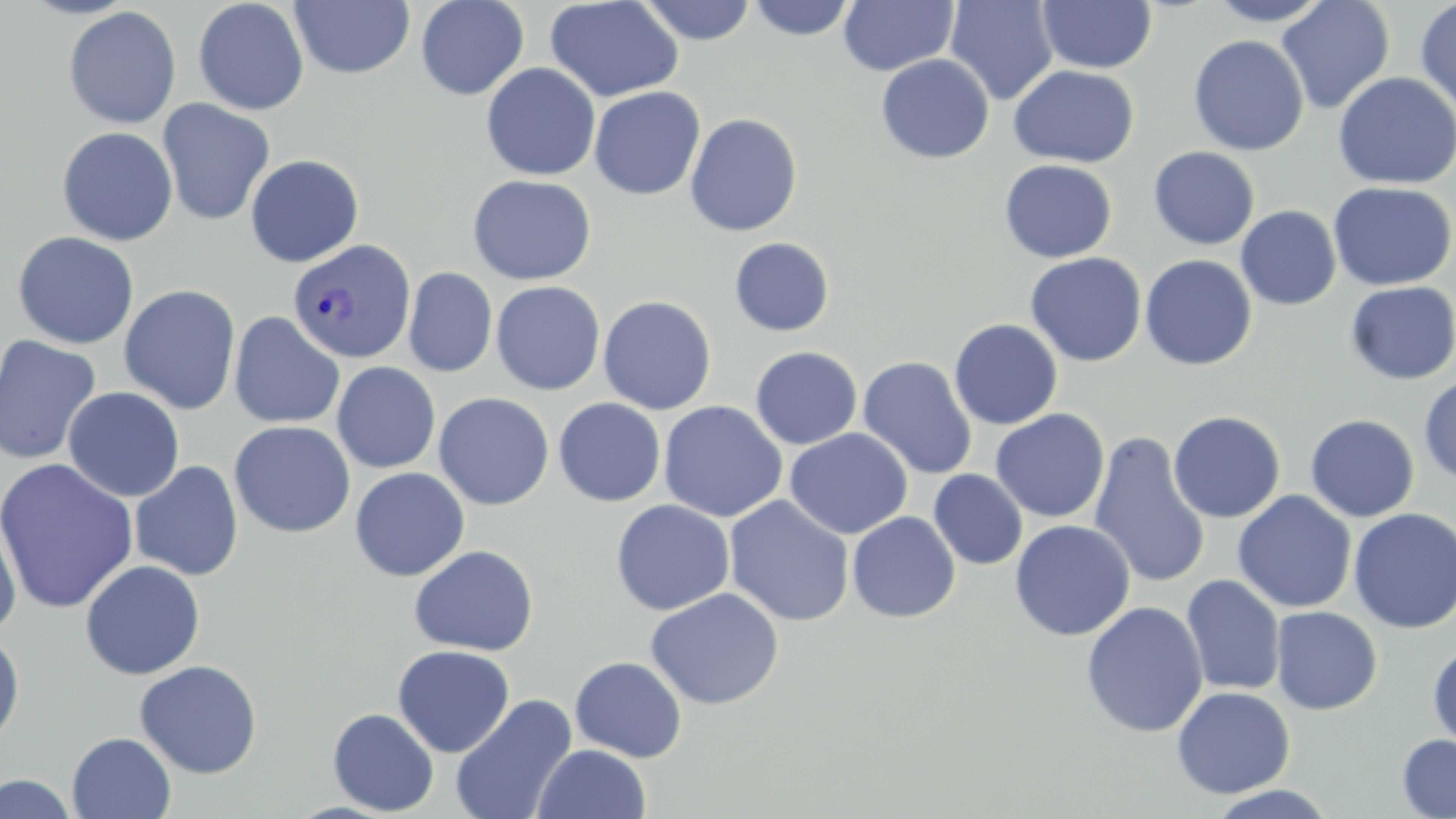

slide-level diagnosis = Plasmodium vivax
image size = 1456×819 pixels
stain = May-Grünwald-Giemsa
preparation = thin blood smear
modality = light microscopy
field of view = single
uninfected red blood cell locations = approximate bounding boxes as named x1/y1/x2/y2 corners in pixels: (x1=193, y1=0, x2=310, y2=116), (x1=415, y1=0, x2=529, y2=100), (x1=545, y1=0, x2=684, y2=103), (x1=638, y1=0, x2=757, y2=45), (x1=746, y1=0, x2=857, y2=41), (x1=944, y1=0, x2=1058, y2=106), (x1=1037, y1=0, x2=1157, y2=74), (x1=1204, y1=0, x2=1335, y2=26), (x1=1275, y1=0, x2=1395, y2=114), (x1=1415, y1=0, x2=1456, y2=117), (x1=289, y1=1, x2=415, y2=80), (x1=838, y1=1, x2=958, y2=76), (x1=63, y1=6, x2=182, y2=129), (x1=1188, y1=34, x2=1309, y2=155), (x1=876, y1=54, x2=995, y2=164), (x1=481, y1=62, x2=601, y2=181), (x1=1008, y1=65, x2=1140, y2=167), (x1=1332, y1=71, x2=1456, y2=190), (x1=589, y1=86, x2=706, y2=200), (x1=156, y1=99, x2=276, y2=227), (x1=684, y1=113, x2=803, y2=237), (x1=56, y1=126, x2=178, y2=246), (x1=1148, y1=146, x2=1260, y2=250), (x1=245, y1=153, x2=365, y2=267), (x1=999, y1=159, x2=1118, y2=264), (x1=467, y1=174, x2=596, y2=285), (x1=1327, y1=181, x2=1456, y2=291), (x1=1235, y1=205, x2=1342, y2=310), (x1=12, y1=231, x2=139, y2=350), (x1=729, y1=237, x2=835, y2=336), (x1=1025, y1=252, x2=1147, y2=366), (x1=1139, y1=254, x2=1257, y2=371), (x1=403, y1=267, x2=498, y2=377), (x1=491, y1=281, x2=606, y2=395), (x1=1345, y1=281, x2=1455, y2=385), (x1=119, y1=284, x2=241, y2=415), (x1=597, y1=295, x2=717, y2=415), (x1=228, y1=311, x2=345, y2=429), (x1=949, y1=318, x2=1063, y2=430), (x1=0, y1=334, x2=102, y2=466), (x1=749, y1=346, x2=863, y2=450), (x1=857, y1=356, x2=977, y2=480), (x1=332, y1=361, x2=441, y2=474), (x1=1418, y1=375, x2=1456, y2=486), (x1=63, y1=387, x2=185, y2=502), (x1=433, y1=392, x2=554, y2=511), (x1=553, y1=398, x2=666, y2=506), (x1=657, y1=401, x2=788, y2=522), (x1=990, y1=408, x2=1110, y2=523), (x1=1168, y1=410, x2=1285, y2=523), (x1=1305, y1=414, x2=1420, y2=522), (x1=229, y1=420, x2=355, y2=538), (x1=784, y1=428, x2=913, y2=539), (x1=1088, y1=430, x2=1211, y2=590), (x1=0, y1=457, x2=139, y2=614), (x1=129, y1=461, x2=244, y2=581), (x1=350, y1=467, x2=470, y2=581), (x1=928, y1=469, x2=1028, y2=570), (x1=1231, y1=490, x2=1356, y2=613), (x1=724, y1=495, x2=855, y2=627), (x1=611, y1=499, x2=735, y2=615), (x1=1348, y1=508, x2=1456, y2=633), (x1=847, y1=511, x2=961, y2=623), (x1=0, y1=513, x2=22, y2=636), (x1=1009, y1=519, x2=1135, y2=642), (x1=408, y1=544, x2=539, y2=656), (x1=80, y1=560, x2=205, y2=680), (x1=1180, y1=574, x2=1286, y2=696), (x1=645, y1=588, x2=784, y2=710), (x1=1081, y1=601, x2=1209, y2=737), (x1=1271, y1=606, x2=1382, y2=715), (x1=0, y1=629, x2=25, y2=748), (x1=1427, y1=641, x2=1456, y2=752), (x1=393, y1=644, x2=515, y2=757), (x1=570, y1=656, x2=688, y2=762), (x1=135, y1=660, x2=263, y2=779), (x1=1171, y1=686, x2=1296, y2=798), (x1=450, y1=694, x2=578, y2=819), (x1=328, y1=708, x2=439, y2=816), (x1=67, y1=732, x2=176, y2=818), (x1=1397, y1=733, x2=1456, y2=818), (x1=533, y1=744, x2=651, y2=819), (x1=0, y1=772, x2=80, y2=818), (x1=1204, y1=785, x2=1341, y2=818)
magnification = 1000x
Plasmodium vivax-infected red blood cell locations = approximate bounding boxes as named x1/y1/x2/y2 corners in pixels: (x1=287, y1=237, x2=417, y2=363)